Locate every Babesia divergens-infected red blood cell.
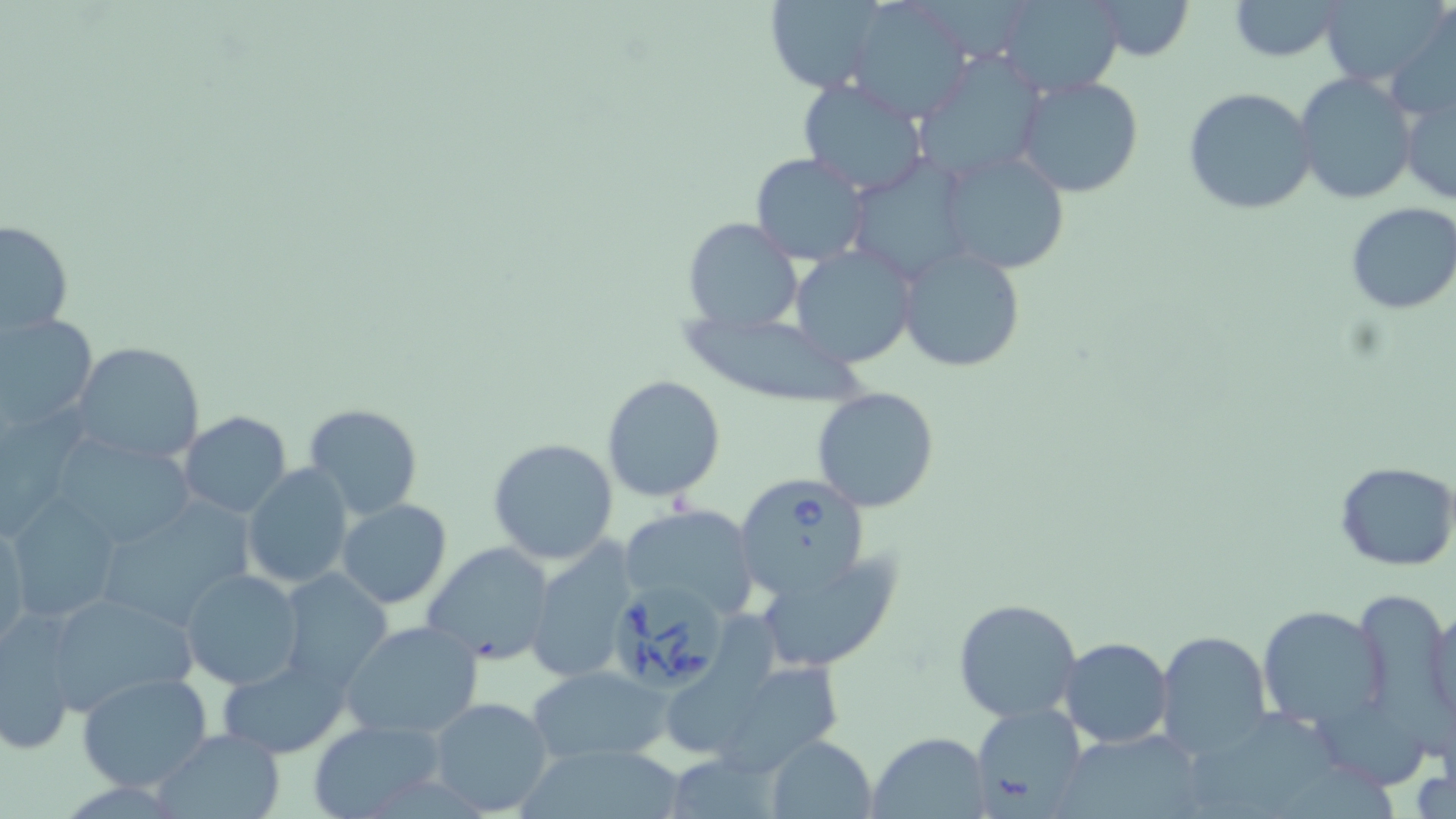

Approximate bounding boxes as [x1, y1, x2, y2] in pixels.
Babesia divergens-infected red blood cells: [733, 472, 872, 597], [605, 583, 732, 696].

Summary:
  - Uninfected red blood cell locations: [758, 0, 888, 91], [997, 0, 1127, 97], [1088, 0, 1196, 62], [1228, 0, 1344, 62], [1321, 0, 1449, 93], [847, 3, 973, 117], [914, 50, 1049, 180], [1294, 72, 1418, 207], [1013, 75, 1143, 199], [795, 76, 931, 195], [1400, 82, 1456, 205], [1184, 86, 1318, 215], [935, 150, 1069, 272], [749, 153, 871, 264], [861, 158, 967, 284], [1344, 202, 1456, 314], [681, 216, 804, 336], [2, 217, 74, 339], [789, 244, 916, 369], [897, 247, 1025, 373], [0, 312, 97, 433], [679, 312, 871, 405], [70, 342, 205, 465], [602, 375, 725, 500], [811, 387, 941, 513], [302, 403, 424, 521], [179, 411, 293, 517], [49, 435, 196, 549], [487, 437, 621, 564], [1334, 461, 1456, 569], [242, 463, 353, 590], [9, 499, 123, 626], [337, 499, 452, 609], [92, 500, 254, 631], [619, 503, 759, 620], [1, 518, 28, 651], [524, 538, 641, 683], [424, 542, 556, 665], [756, 553, 901, 672], [179, 568, 305, 691], [279, 570, 394, 693], [1350, 585, 1451, 716], [42, 590, 198, 716], [952, 597, 1084, 724], [1426, 600, 1456, 739], [1256, 604, 1388, 732], [668, 610, 779, 755], [1, 616, 80, 754], [340, 620, 484, 740], [1156, 631, 1272, 757], [1059, 637, 1173, 749], [214, 657, 353, 757], [723, 662, 855, 772], [527, 666, 672, 764], [76, 672, 214, 792], [1195, 695, 1334, 816], [427, 697, 556, 816], [1312, 699, 1436, 788], [974, 704, 1088, 812], [307, 718, 444, 819], [151, 727, 287, 818], [870, 730, 987, 818], [1072, 732, 1208, 819], [766, 734, 878, 816], [515, 746, 687, 819], [667, 747, 790, 819], [1294, 759, 1401, 818]
  - Slide-level diagnosis: Babesia divergens
  - Image size: 1456×819 pixels
  - Stain: May-Grünwald-Giemsa
  - Field of view: single
  - Preparation: thin blood film
  - Magnification: 1000x
  - Modality: optical microscopy